Locate every Plasmodium ovale-infected red blood cell.
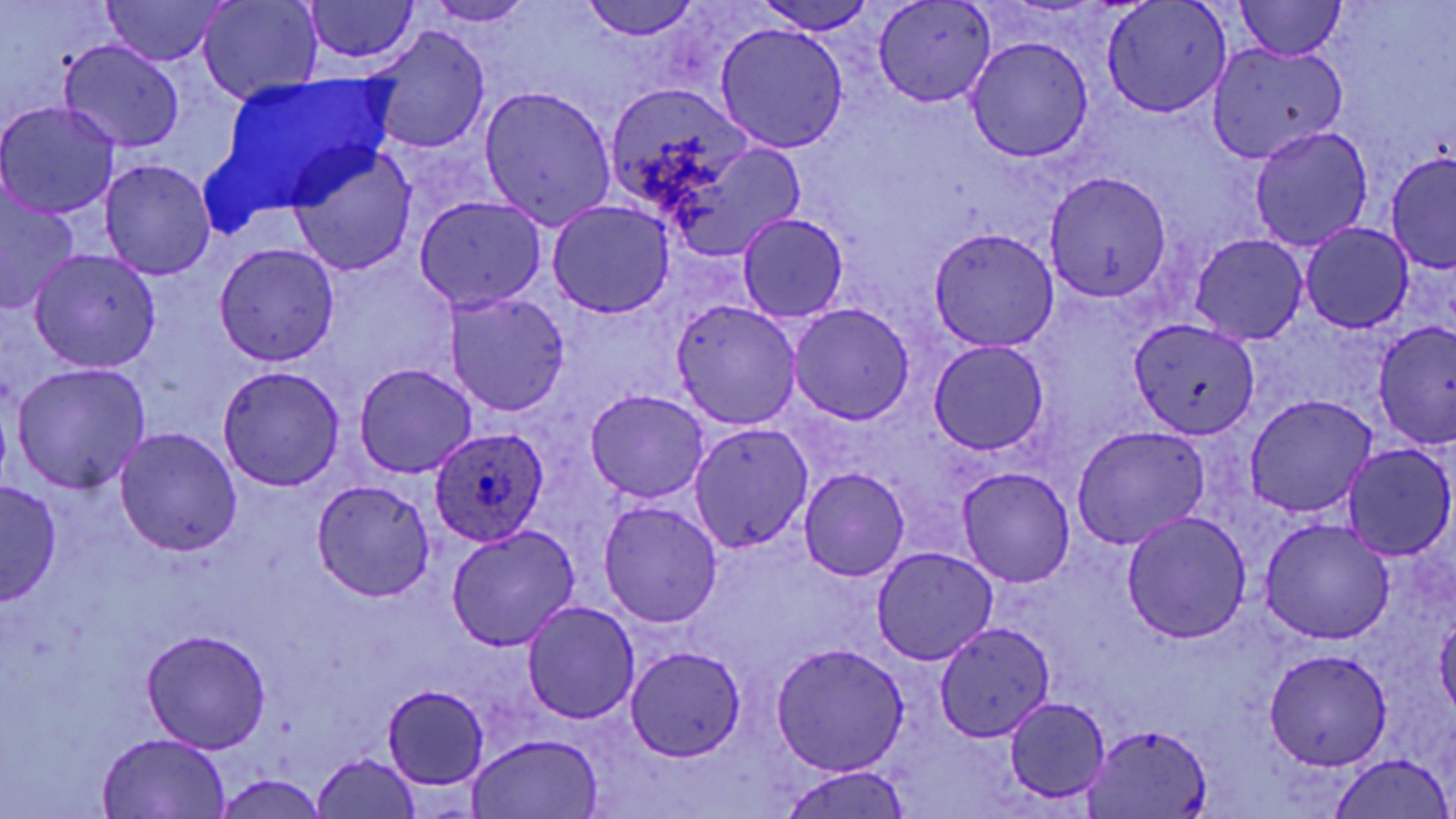

Approximate bounding boxes as [x1, y1, x2, y2] in pixels.
Plasmodium ovale-infected red blood cells: [427, 425, 551, 548].

Summary:
  - Uninfected red blood cell locations: [97, 0, 232, 66], [197, 0, 325, 103], [300, 0, 424, 70], [580, 0, 704, 43], [753, 0, 881, 35], [871, 0, 999, 111], [1099, 0, 1235, 120], [420, 1, 541, 28], [1231, 1, 1350, 60], [714, 21, 848, 156], [369, 24, 494, 156], [965, 36, 1096, 164], [56, 38, 186, 154], [1204, 41, 1349, 165], [604, 81, 753, 215], [474, 83, 619, 228], [0, 100, 120, 222], [1247, 125, 1375, 251], [658, 127, 806, 264], [288, 143, 415, 277], [1386, 149, 1456, 278], [98, 157, 219, 280], [1044, 170, 1174, 304], [0, 183, 80, 316], [412, 194, 547, 313], [545, 198, 675, 317], [735, 212, 849, 323], [1298, 222, 1416, 335], [925, 224, 1061, 354], [1188, 232, 1309, 345], [213, 243, 339, 367], [28, 249, 159, 373], [441, 290, 571, 417], [669, 302, 806, 431], [786, 302, 917, 425], [1128, 318, 1261, 441], [1374, 321, 1454, 452], [926, 337, 1052, 458], [9, 360, 151, 494], [353, 362, 478, 480], [216, 364, 349, 493], [583, 389, 709, 505], [1241, 393, 1381, 519], [687, 420, 812, 553], [115, 426, 242, 554], [1070, 426, 1211, 550], [1342, 442, 1454, 562], [796, 465, 914, 582], [956, 466, 1075, 587], [2, 480, 61, 602], [310, 480, 437, 601], [596, 497, 725, 630], [1119, 509, 1252, 643], [1258, 516, 1396, 645], [444, 522, 584, 652], [869, 543, 998, 667], [519, 598, 641, 723], [931, 620, 1055, 744], [143, 627, 271, 750], [770, 640, 911, 777], [624, 645, 749, 761], [1261, 646, 1395, 771], [381, 685, 492, 789], [1000, 695, 1113, 804], [1080, 719, 1216, 819], [97, 731, 230, 817], [468, 731, 603, 818], [313, 753, 423, 819], [1329, 754, 1452, 818], [776, 766, 914, 819], [212, 775, 329, 818]
  - Slide-level diagnosis: Plasmodium ovale
  - Field of view: single
  - Magnification: 1000x
  - Modality: optical microscopy
  - Stain: May-Grünwald-Giemsa
  - Preparation: thin blood smear
  - Image size: 1456×819 pixels